Locate every blood parasite and identify its species.
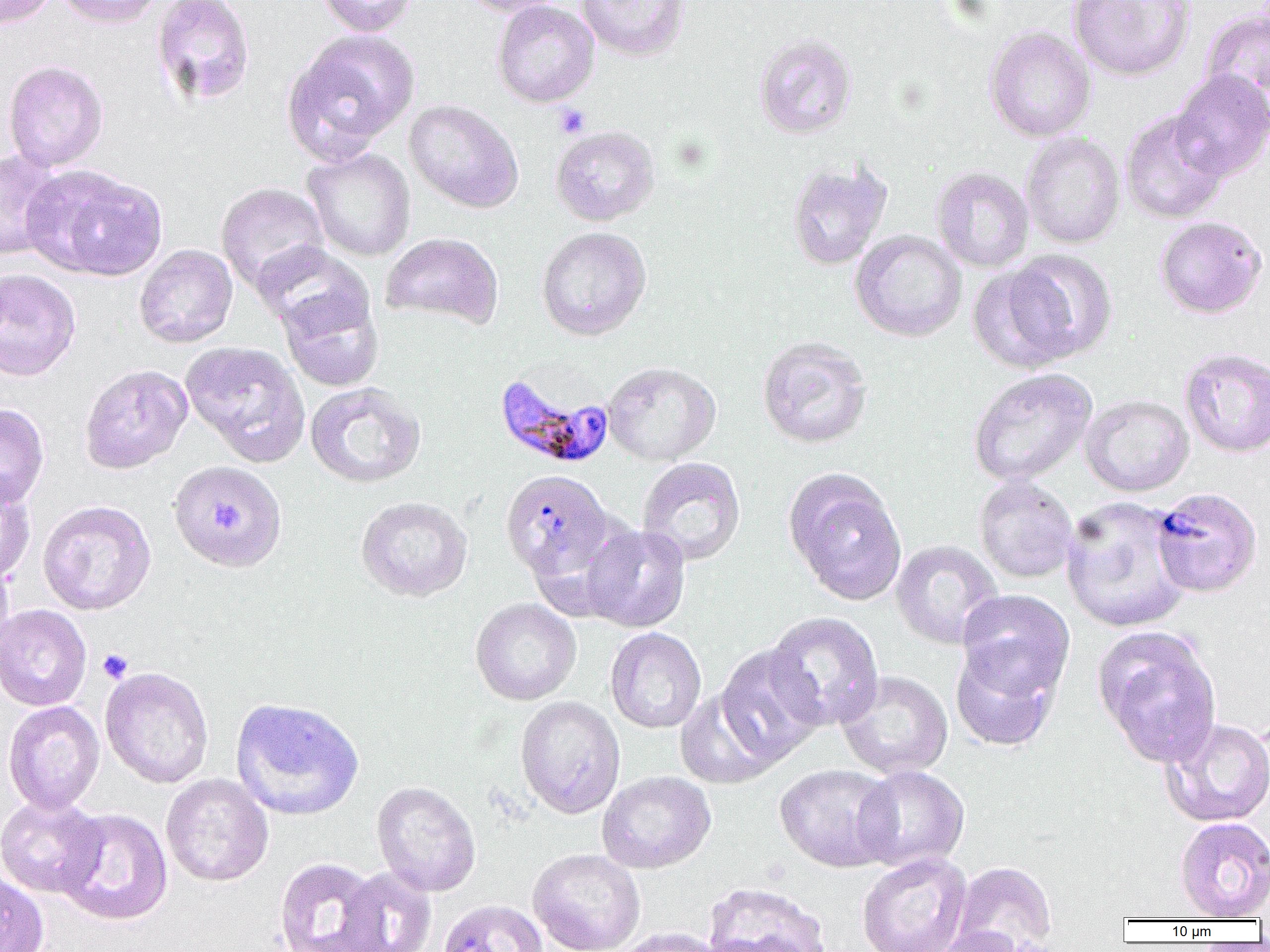
Approximate bounding boxes as (x1, y1, x2, y2) in pixels.
Plasmodium falciparum-infected red blood cells: (494, 368, 615, 470), (504, 476, 617, 580).
No Plasmodium ovale, Plasmodium malariae, Plasmodium vivax, Babesia divergens, or Trypanosoma brucei observed.

Summary:
  - Platelet locations: (554, 104, 590, 138), (209, 504, 248, 534), (97, 649, 133, 683)
  - Uninfected red blood cell locations: (0, 0, 58, 28), (55, 0, 164, 28), (151, 0, 255, 106), (317, 0, 419, 37), (461, 0, 569, 17), (576, 0, 690, 61), (1068, 0, 1196, 81), (491, 1, 599, 108), (1202, 6, 1270, 117), (984, 26, 1096, 142), (282, 31, 418, 161), (754, 32, 858, 139), (3, 60, 108, 172), (1169, 70, 1270, 182), (404, 100, 524, 213), (1120, 111, 1229, 224), (550, 125, 660, 226), (1021, 132, 1125, 249), (302, 147, 416, 262), (0, 149, 66, 262), (787, 161, 892, 270), (26, 165, 166, 280), (931, 167, 1034, 273), (215, 182, 329, 292), (1154, 216, 1267, 319), (536, 226, 652, 340), (850, 229, 967, 342), (381, 232, 503, 329), (252, 242, 372, 340), (134, 244, 237, 348), (1003, 249, 1118, 364), (968, 263, 1077, 374), (0, 267, 81, 381), (278, 287, 384, 392), (756, 336, 873, 449), (180, 340, 310, 466), (1179, 346, 1270, 458), (603, 361, 721, 465), (79, 364, 193, 473), (968, 368, 1097, 487), (304, 382, 426, 488), (1080, 394, 1194, 496), (0, 403, 49, 508), (637, 457, 746, 566), (171, 464, 291, 577), (783, 468, 907, 605), (0, 475, 37, 585), (973, 475, 1078, 584), (1151, 488, 1263, 598), (355, 496, 473, 602), (1061, 496, 1192, 634), (37, 500, 156, 615), (581, 523, 691, 633), (891, 540, 1004, 649), (0, 557, 14, 660), (956, 589, 1075, 700), (470, 597, 581, 705), (0, 604, 91, 712), (764, 611, 884, 731), (1092, 624, 1222, 766), (605, 627, 706, 734), (950, 644, 1061, 753), (715, 645, 826, 765), (100, 666, 214, 788), (836, 670, 953, 779), (674, 690, 779, 789), (230, 696, 364, 821), (515, 696, 625, 819), (3, 701, 105, 815), (1160, 717, 1270, 827), (774, 763, 900, 872), (853, 765, 970, 873), (597, 770, 716, 874), (161, 773, 274, 886), (371, 781, 481, 897), (0, 795, 107, 899), (55, 808, 173, 925), (1174, 816, 1270, 921), (528, 848, 646, 952), (856, 852, 972, 952), (274, 856, 387, 952), (951, 861, 1058, 952), (336, 866, 437, 952), (0, 868, 49, 952), (702, 881, 832, 952), (438, 899, 548, 952), (933, 926, 1035, 952), (612, 927, 728, 952)
  - Slide-level diagnosis: Plasmodium falciparum
  - Magnification: 1000x
  - Field of view: one of a larger specimen
  - Image size: 1270×952 pixels
  - Preparation: thin blood smear
  - Modality: optical microscopy